Assess this cell for malaria.
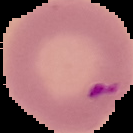
Parasitized.

image_size: 133×133 pixels
image_type: cell region segmented out of the field of view; surrounding area masked to black
preparation: thin blood film